Name the parasite shown.
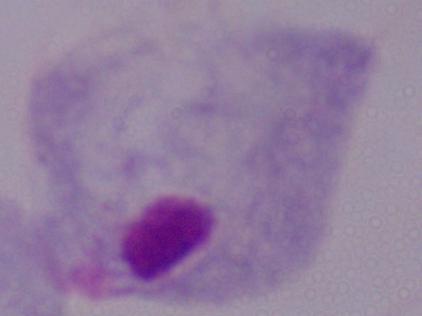
This is a trichomonad.

{
  "magnification": "1000x",
  "modality": "micrograph"
}